Give the position of every Plasmodium falciparum parasite, noting its life-cycle stage.
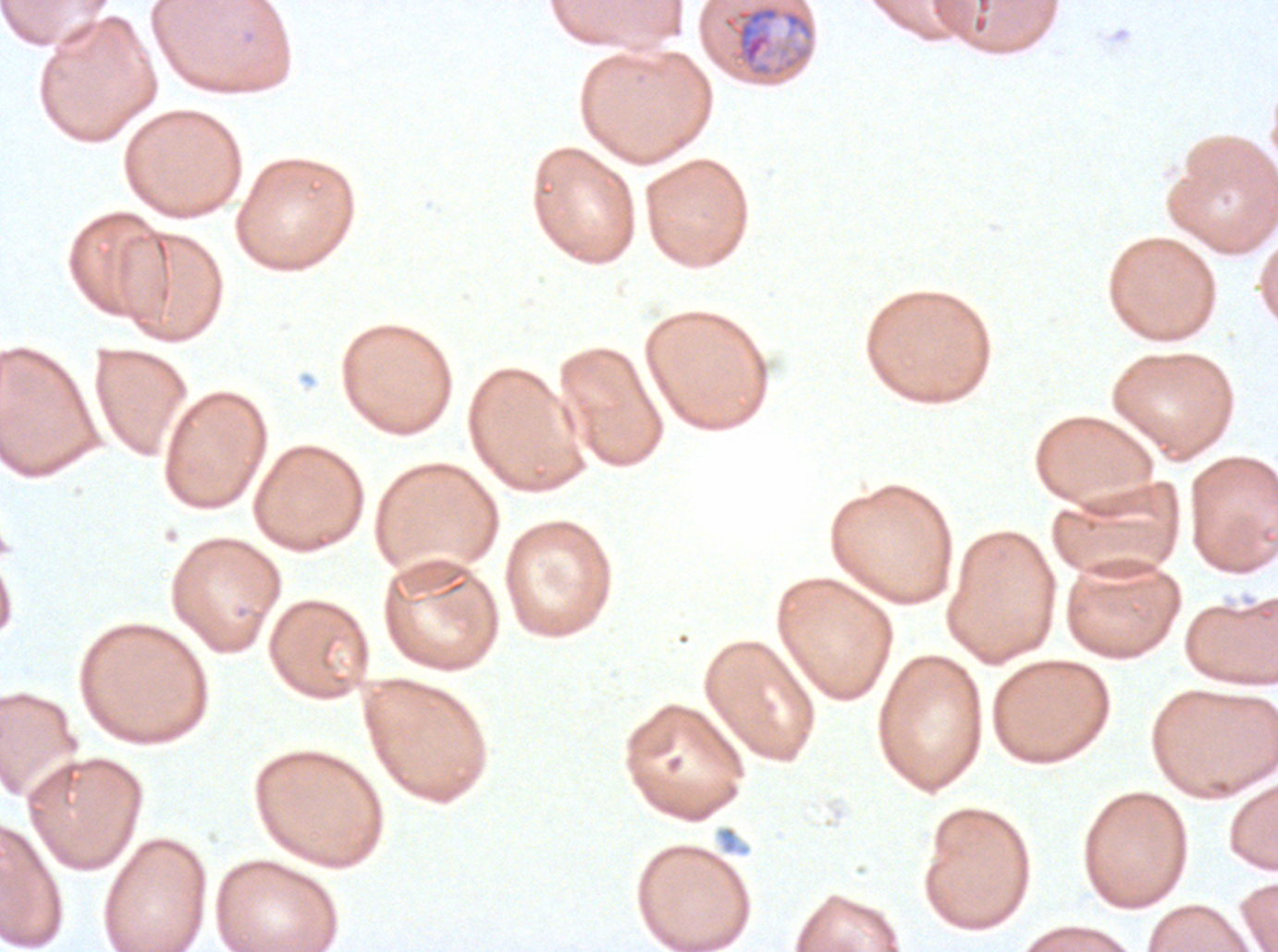
Approximate bounding rectangles given as corner coordinates in pixels from the top-left.
Mid trophozoites: (x1=720, y1=1, x2=817, y2=79).
No rings, late-ring/early-trophozoite forms, late trophozoites, early schizonts, late schizonts, segmenters, or gametocytes observed.

specimen = Plasmodium falciparum cultured ex vivo for 24 to 48 hours, from a patient in The Gambia
field of view = sub-image separated from a larger composite
stain = Giemsa
image size = 1278×952 pixels
preparation = thin blood smear